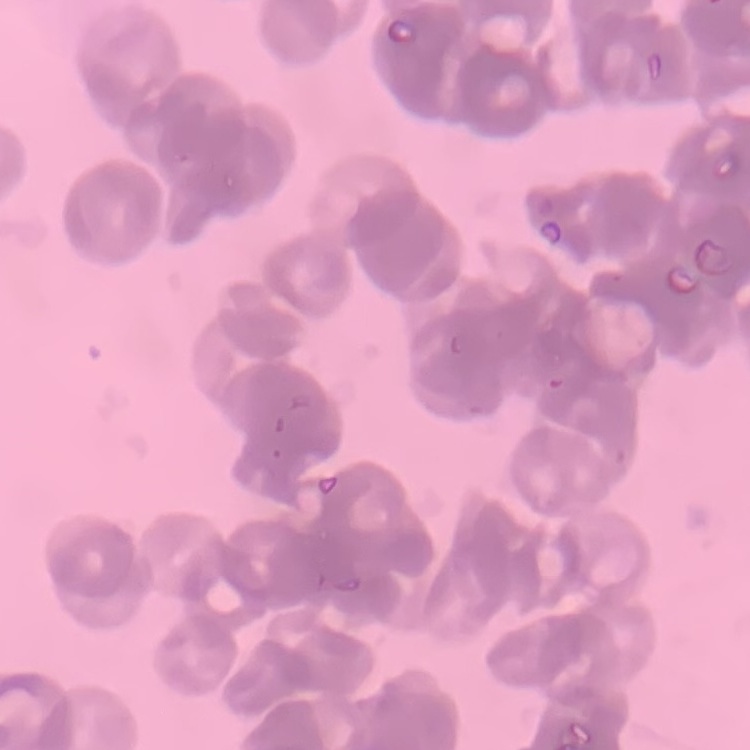

The red blood cells show rouleaux formation. Square crop of a larger photomicrograph. Thin blood smear. Field's or Giemsa stain.